Locate and identify every blood parasite.
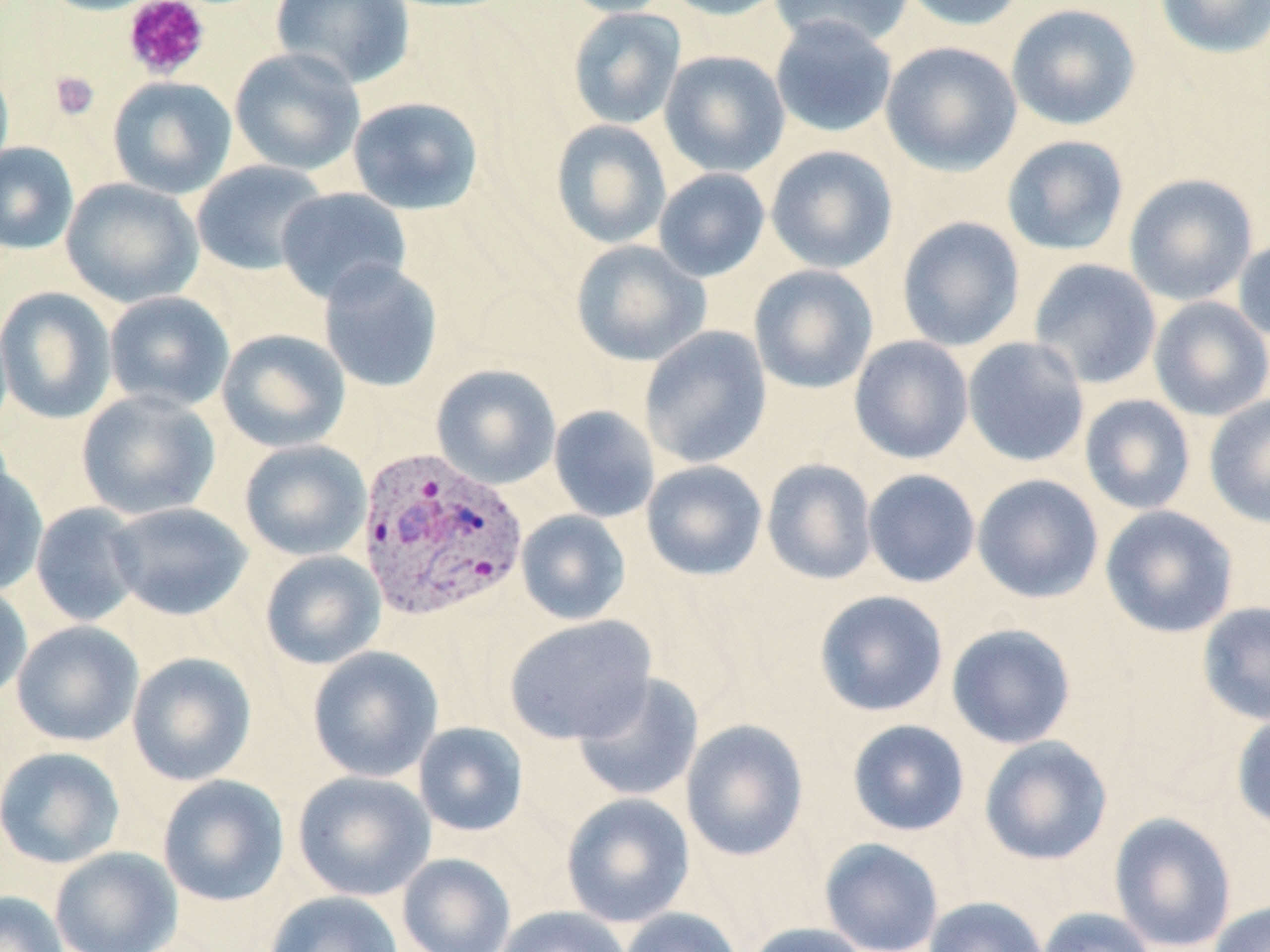
Approximate bounding boxes as (x1, y1, x2, y2) in pixels.
Plasmodium vivax-infected red blood cells: (356, 447, 526, 623).
No Plasmodium falciparum, Plasmodium ovale, Plasmodium malariae, Babesia divergens, or Trypanosoma brucei observed.

slide-level diagnosis = Plasmodium vivax
stain = May-Grünwald-Giemsa
preparation = thin blood film
field of view = single
magnification = 1000x
image size = 1270×952 pixels
platelet locations = approximate bounding boxes as (x1, y1, x2, y2) in pixels: (122, 0, 211, 81), (49, 70, 99, 120)
uninfected red blood cell locations = approximate bounding boxes as (x1, y1, x2, y2) in pixels: (36, 0, 166, 16), (556, 0, 676, 17), (659, 0, 790, 20), (770, 0, 914, 50), (898, 0, 1029, 31), (1154, 0, 1270, 59), (270, 1, 415, 88), (1006, 3, 1141, 130), (567, 7, 686, 129), (770, 15, 898, 138), (880, 41, 1022, 176), (229, 47, 366, 176), (659, 50, 790, 177), (0, 58, 14, 180), (107, 75, 237, 199), (347, 96, 484, 215), (550, 120, 672, 249), (1002, 135, 1130, 256), (0, 142, 79, 255), (765, 145, 897, 273), (191, 160, 328, 276), (653, 168, 770, 282), (1124, 173, 1258, 306), (61, 178, 204, 308), (276, 187, 411, 304), (897, 216, 1026, 352), (1233, 235, 1270, 342), (570, 239, 711, 366), (1028, 258, 1162, 389), (318, 259, 443, 393), (749, 264, 878, 394), (0, 286, 117, 424), (104, 291, 235, 413), (1149, 296, 1270, 422), (639, 326, 772, 469), (216, 328, 351, 452), (849, 335, 974, 464), (962, 337, 1090, 468), (431, 364, 561, 489), (76, 389, 220, 521), (1079, 394, 1196, 515), (1204, 394, 1270, 529), (548, 405, 660, 523), (239, 439, 372, 561), (762, 459, 878, 585), (641, 460, 767, 581), (0, 461, 48, 596), (862, 469, 981, 587), (972, 474, 1104, 603), (30, 502, 145, 627), (107, 502, 253, 621), (1099, 505, 1239, 638), (516, 510, 631, 625), (260, 550, 386, 670), (0, 582, 33, 705), (814, 589, 948, 717), (1197, 601, 1270, 725), (503, 614, 657, 745), (11, 620, 144, 747), (946, 623, 1077, 749), (307, 645, 443, 782), (127, 652, 257, 786), (572, 673, 704, 803), (1231, 711, 1270, 833), (681, 718, 809, 861), (847, 719, 970, 836), (413, 721, 529, 837), (979, 735, 1113, 865), (0, 746, 125, 868), (293, 770, 436, 902), (157, 774, 289, 906), (560, 792, 695, 928), (1108, 812, 1237, 951), (819, 838, 944, 952), (50, 846, 183, 952), (396, 852, 516, 952), (0, 890, 68, 952), (264, 890, 404, 952), (923, 896, 1049, 952), (1207, 900, 1270, 952), (495, 906, 632, 952), (618, 907, 744, 952), (1036, 907, 1157, 952), (744, 922, 870, 952)
modality = light microscopy